Name the cell type shown.
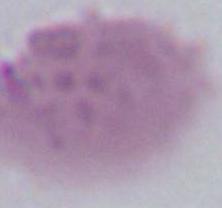

An erythrocyte.

{
  "magnification": "1000x",
  "modality": "photomicrograph"
}